Report the malaria status of this cell.
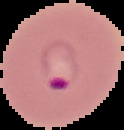
It is parasitized.

preparation = thin blood film
image size = 124×130 pixels
image type = cell region segmented out of the field of view; surrounding area masked to black